Classify this cell by malaria status.
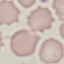

Uninfected.

capture: smartphone through the microscope eyepiece
stain: Giemsa
image_type: automatically extracted cell patch, resized to 64 × 64 pixels
preparation: thin blood film